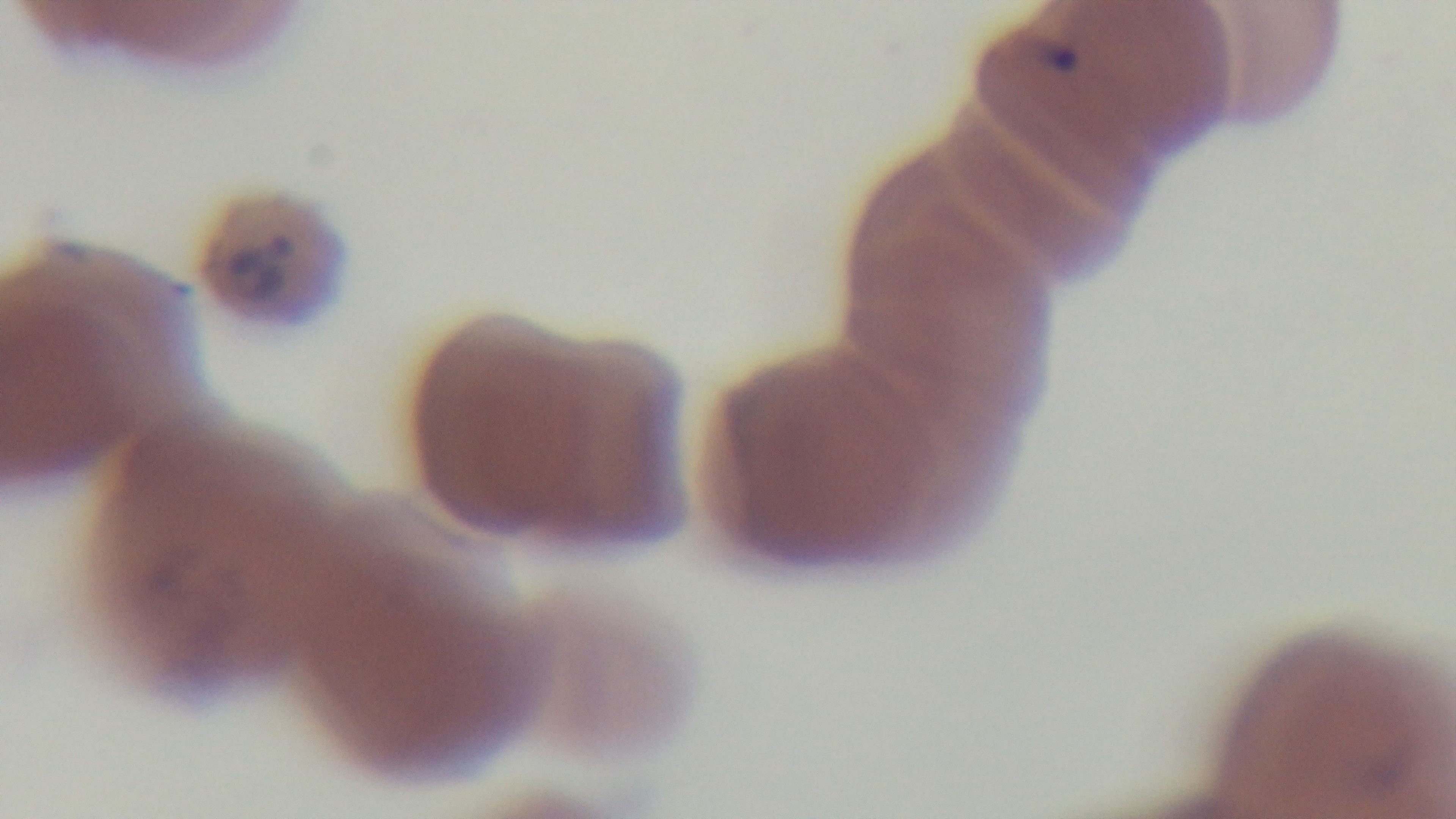 Single field of view. Malaria status: positive. Photomicrograph. Oil-immersion objective, 100x. Giemsa-stained. Preparation: thin. Mounted 4K digital camera.